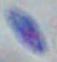

magnification: 1000x
modality: photomicrograph
identification: Toxoplasma gondii